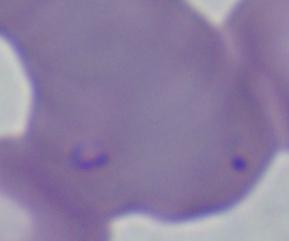

A Babesia parasite is shown. 1000x magnification. Photomicrograph.